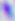 400x magnification. Toxoplasma gondii is seen. Micrograph.